Locate every Plasmodium falciparum-infected red blood cell.
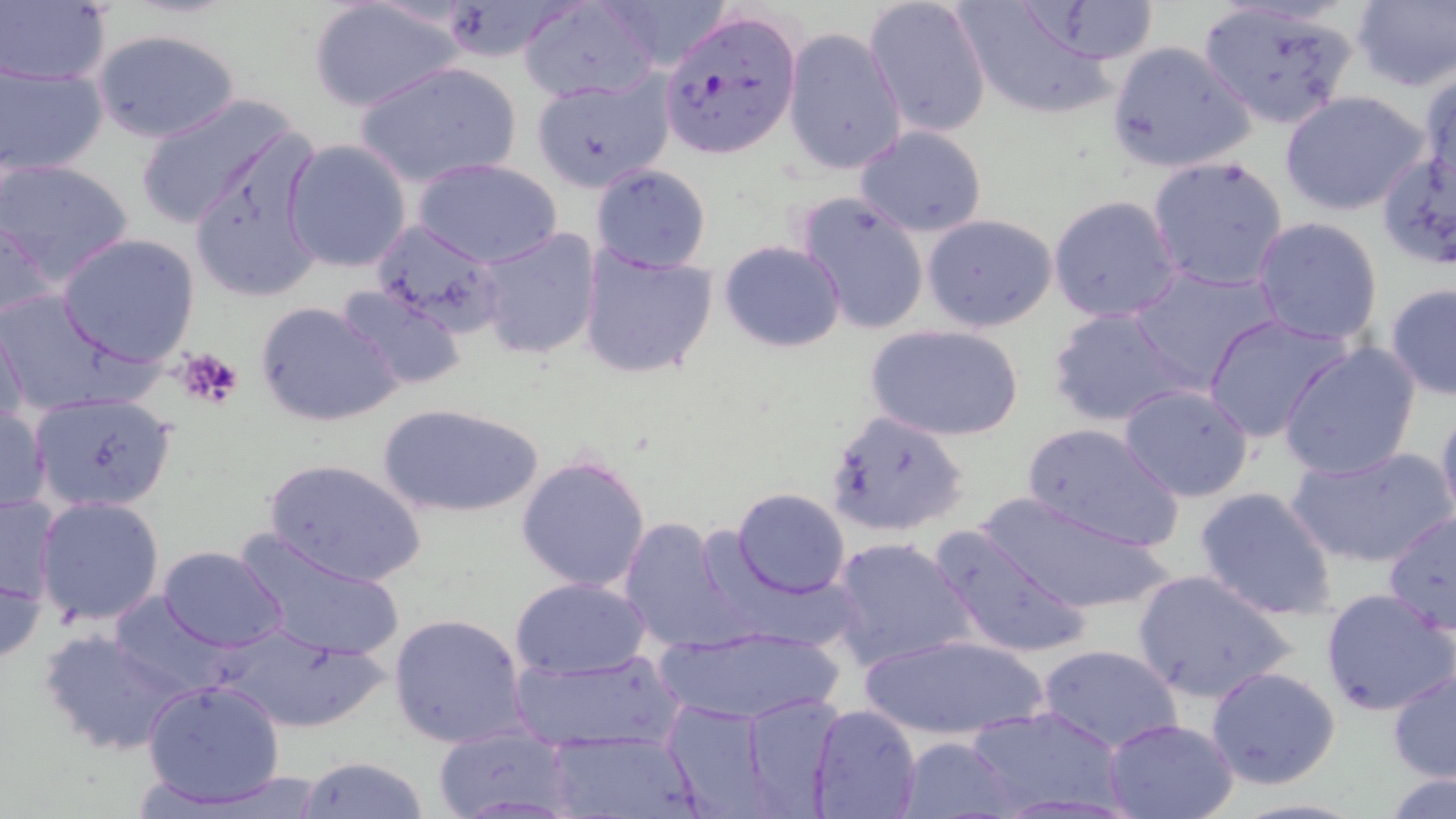
Approximate bounding boxes as [x1, y1, x2, y2] in pixels.
Plasmodium falciparum-infected red blood cells (subset): [657, 8, 800, 157].

slide-level diagnosis = Plasmodium falciparum
uninfected red blood cell locations (subset) = approximate bounding boxes as [x1, y1, x2, y2] in pixels: [306, 0, 466, 114], [595, 0, 737, 71], [863, 0, 992, 136], [1348, 0, 1456, 91], [953, 1, 1129, 124], [1, 2, 111, 86], [519, 2, 661, 101], [1196, 3, 1361, 130], [92, 27, 242, 143], [783, 27, 907, 177], [1107, 40, 1258, 175], [353, 60, 522, 189], [2, 63, 108, 176], [1418, 68, 1456, 197], [1280, 90, 1432, 216], [135, 93, 304, 229], [854, 125, 988, 237], [187, 131, 327, 303], [283, 139, 411, 273], [1375, 150, 1456, 276], [1147, 156, 1290, 292], [1, 159, 135, 290], [413, 159, 562, 268], [588, 162, 713, 273], [794, 192, 930, 337], [1048, 195, 1184, 322], [1, 212, 59, 328], [921, 213, 1058, 333], [1251, 216, 1384, 344], [364, 217, 506, 350], [474, 228, 603, 360], [56, 234, 200, 366], [718, 239, 847, 353], [576, 245, 718, 380], [1129, 264, 1281, 394], [1385, 283, 1456, 400], [334, 285, 468, 393], [0, 289, 146, 418], [255, 300, 404, 429], [1045, 306, 1196, 428], [1203, 314, 1356, 444], [0, 316, 29, 430], [865, 322, 1027, 442], [1279, 341, 1424, 480], [1118, 385, 1256, 502], [26, 391, 180, 514], [1435, 400, 1456, 527], [0, 402, 50, 517], [377, 403, 544, 518], [825, 408, 971, 539], [1022, 421, 1185, 551], [1286, 444, 1452, 570], [515, 454, 651, 594], [262, 457, 427, 588], [1192, 485, 1340, 623], [731, 488, 852, 597], [0, 492, 62, 608], [970, 492, 1176, 618], [35, 495, 166, 627], [1382, 509, 1456, 636], [618, 519, 750, 654], [929, 525, 1093, 663], [235, 531, 406, 662], [829, 536, 976, 672], [157, 545, 290, 652], [0, 561, 46, 666], [1130, 568, 1297, 704], [509, 576, 650, 678], [1320, 589, 1453, 718], [109, 593, 232, 697], [388, 613, 529, 748], [212, 623, 385, 734], [652, 623, 848, 726], [38, 627, 189, 757], [855, 633, 1055, 740], [1036, 643, 1184, 753], [510, 651, 684, 753], [1387, 665, 1456, 784], [1205, 666, 1342, 791], [141, 678, 286, 809], [741, 691, 848, 818], [661, 698, 784, 816], [806, 704, 921, 819], [961, 705, 1129, 817], [1102, 717, 1241, 819], [430, 724, 575, 819], [547, 735, 701, 817], [895, 735, 1017, 819], [298, 756, 429, 818], [1379, 771, 1456, 817]
image size = 1456×819 pixels
magnification = 1000x
field of view = one of a larger specimen
modality = light microscopy
platelet locations = approximate bounding boxes as [x1, y1, x2, y2] in pixels: [177, 346, 243, 412]
preparation = thin blood smear
stain = May-Grünwald-Giemsa